Assess the morphology of the red blood cells.
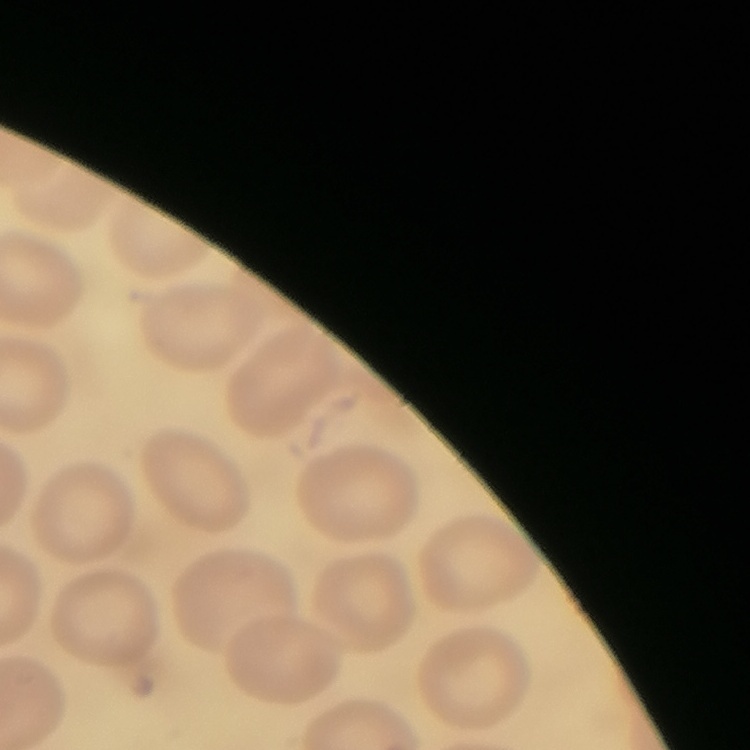
No rouleaux formation.

Summary:
  - Stain: Field's or Giemsa
  - Preparation: thin blood film
  - Image type: square crop of a larger photomicrograph